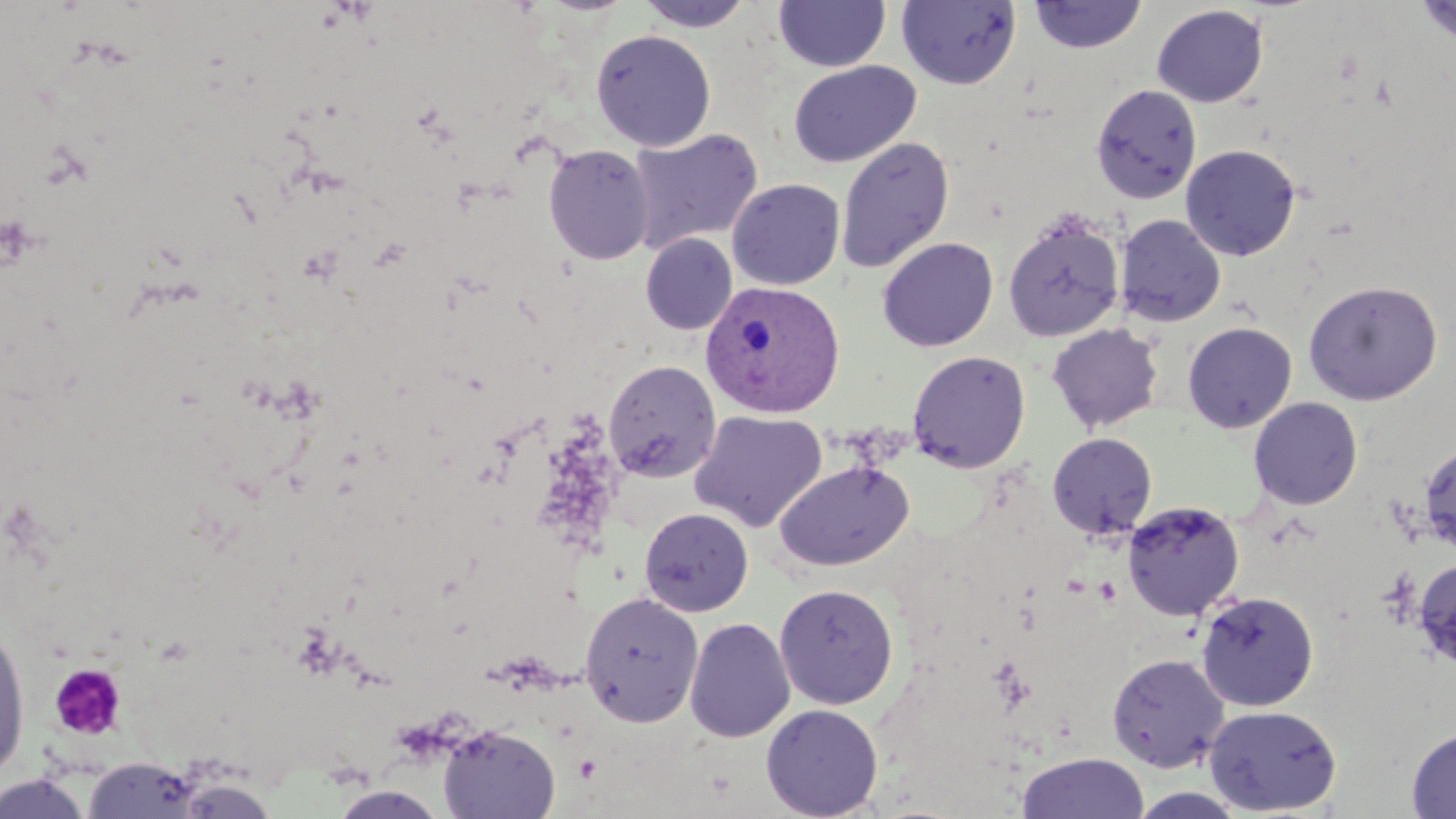
slide_level_diagnosis: Plasmodium vivax
uninfected_red_blood_cell_locations: 'approximate bounding boxes as named x1/y1/x2/y2 corners in pixels: (x1=633, y1=0, x2=755, y2=32), (x1=896, y1=0, x2=1022, y2=90), (x1=1027, y1=0, x2=1147, y2=55), (x1=1413, y1=0, x2=1456, y2=47), (x1=773, y1=1, x2=891, y2=72), (x1=1151, y1=4, x2=1268, y2=107), (x1=590, y1=29, x2=716, y2=151), (x1=788, y1=60, x2=921, y2=168), (x1=1091, y1=83, x2=1202, y2=204), (x1=628, y1=127, x2=763, y2=253), (x1=835, y1=136, x2=955, y2=275), (x1=1180, y1=143, x2=1302, y2=261), (x1=542, y1=144, x2=656, y2=265), (x1=726, y1=178, x2=845, y2=290), (x1=1002, y1=210, x2=1125, y2=343), (x1=1114, y1=214, x2=1227, y2=327), (x1=640, y1=233, x2=737, y2=335), (x1=877, y1=237, x2=998, y2=352), (x1=1302, y1=279, x2=1443, y2=405), (x1=1182, y1=321, x2=1298, y2=434), (x1=1046, y1=323, x2=1164, y2=434), (x1=906, y1=350, x2=1031, y2=473), (x1=604, y1=360, x2=721, y2=482), (x1=1248, y1=396, x2=1363, y2=510), (x1=689, y1=410, x2=827, y2=532), (x1=1047, y1=432, x2=1157, y2=540), (x1=1419, y1=443, x2=1456, y2=556), (x1=773, y1=458, x2=915, y2=572), (x1=1122, y1=499, x2=1245, y2=620), (x1=639, y1=506, x2=754, y2=617), (x1=1412, y1=557, x2=1456, y2=669), (x1=773, y1=583, x2=899, y2=709), (x1=579, y1=590, x2=704, y2=727), (x1=1195, y1=590, x2=1319, y2=712), (x1=684, y1=617, x2=795, y2=742), (x1=0, y1=619, x2=31, y2=781), (x1=1106, y1=652, x2=1230, y2=772), (x1=760, y1=703, x2=884, y2=819), (x1=1203, y1=704, x2=1342, y2=816), (x1=437, y1=723, x2=561, y2=818), (x1=1406, y1=727, x2=1456, y2=818), (x1=1017, y1=752, x2=1149, y2=819), (x1=84, y1=756, x2=204, y2=818), (x1=0, y1=772, x2=93, y2=818), (x1=174, y1=776, x2=278, y2=818), (x1=328, y1=785, x2=450, y2=818), (x1=1126, y1=788, x2=1251, y2=818)'
magnification: 1000x
stain: May-Grünwald-Giemsa
image_size: 1456×819 pixels
platelet_locations: 'approximate bounding boxes as named x1/y1/x2/y2 corners in pixels: (x1=49, y1=663, x2=127, y2=740)'
modality: optical microscopy
plasmodium_vivax_infected_red_blood_cell_locations: 'approximate bounding boxes as named x1/y1/x2/y2 corners in pixels: (x1=700, y1=280, x2=845, y2=418)'
preparation: thin blood smear
field_of_view: one of a larger specimen